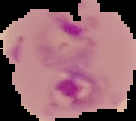 Segmented cell region on a black background. From a thin blood film. Image is 136×121 pixels. Malaria status: parasitized.